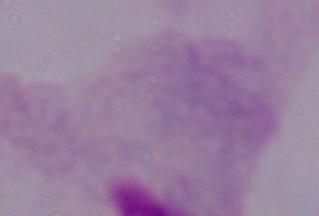

Summary:
  - Modality: photomicrograph
  - Identification: trichomonad
  - Magnification: 1000x